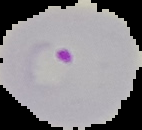

result = Plasmodium parasites identified
image size = 142×130 pixels
image type = cell region segmented out of the field of view; surrounding area masked to black
preparation = thin blood film